State the preparation type.
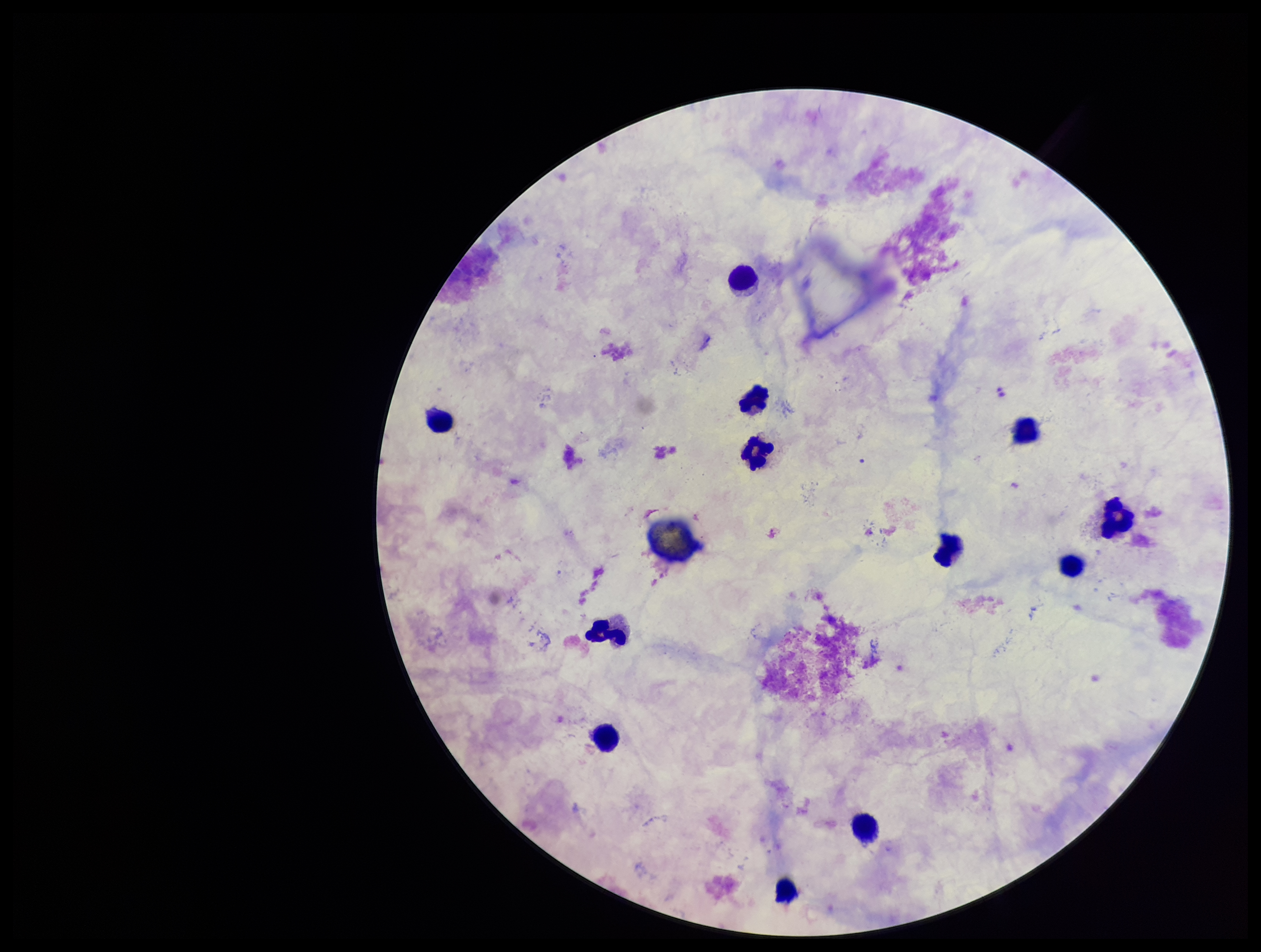

Thick.

capture = smartphone photograph through the microscope eyepiece
stain = Giemsa
field of view = single
Plasmodium parasites = none seen
image size = 1261×952 pixels
parasite count = 0
leukocyte count = 12
patient malaria status = negative